Classify this cell by malaria status.
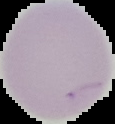

Uninfected.

image size = 115×124 pixels
image type = cell region segmented out of the field of view; surrounding area masked to black
preparation = thin blood film